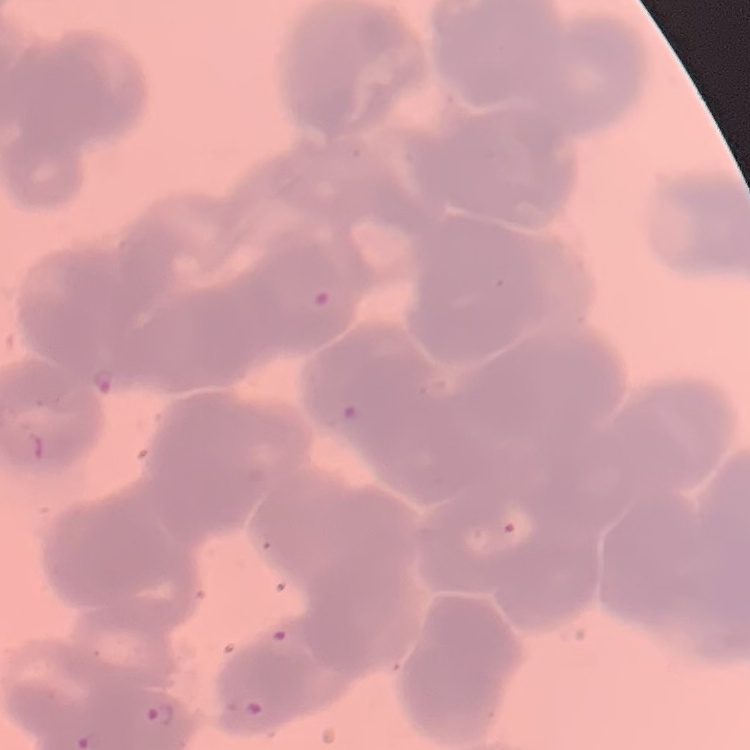
The red blood cells show rouleaux formation. Field's or Giemsa stain. Thin blood film. One tile cut from a larger photomicrograph.